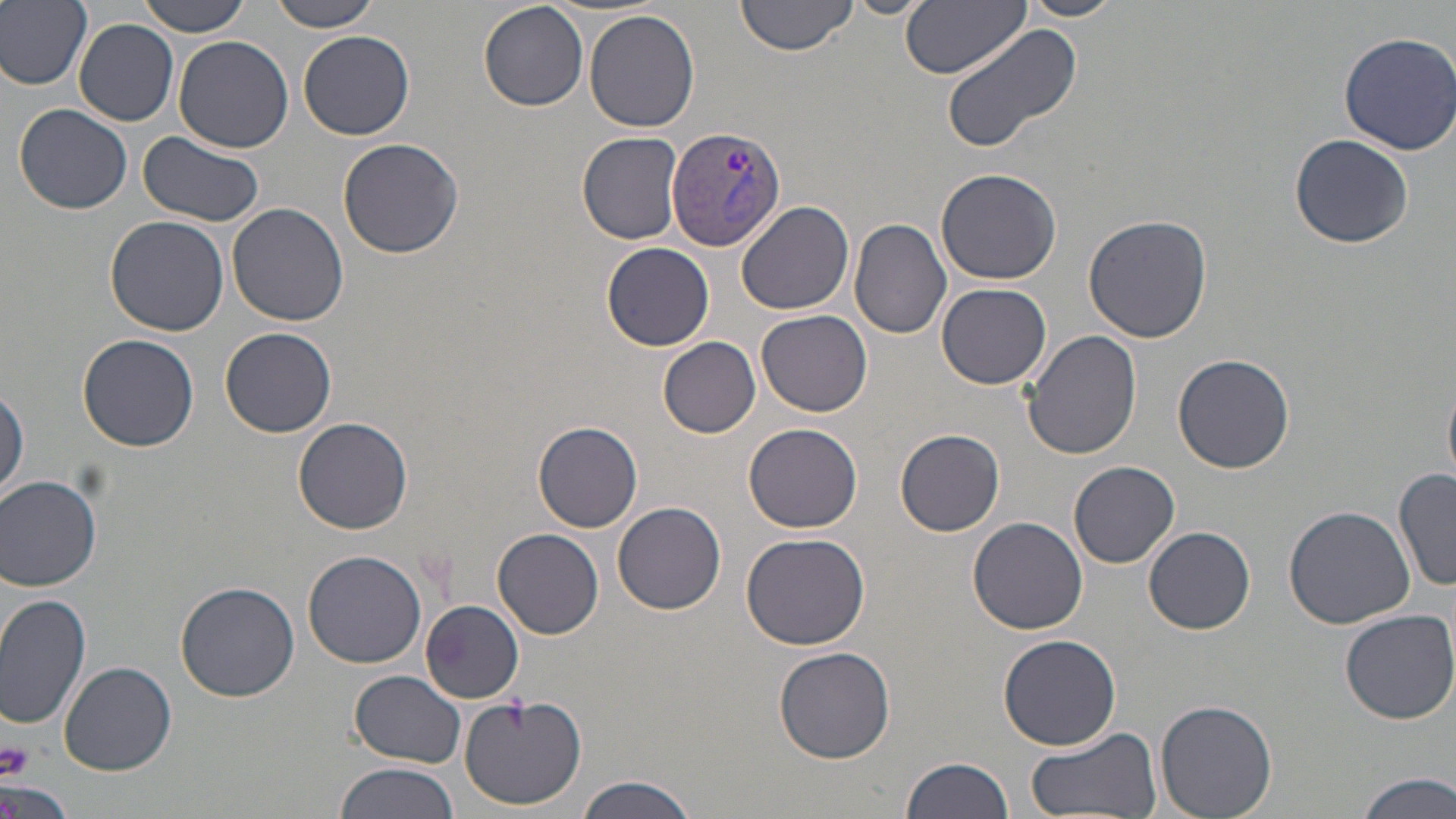

Approximate bounding boxes as (x1,y1)-(x2,y2) corner pairs in pixels. Uninfected red blood cell locations: (0,0)-(93,90), (135,0)-(254,36), (266,0)-(383,32), (736,0)-(858,56), (843,0)-(934,18), (902,0)-(1030,77), (1017,0)-(1128,21), (479,2)-(589,111), (585,8)-(701,133), (75,19)-(179,125), (941,22)-(1087,157), (299,29)-(415,140), (1337,32)-(1454,155), (172,35)-(293,153), (14,104)-(133,215), (139,131)-(267,227), (577,131)-(685,244), (1288,133)-(1414,248), (338,136)-(466,259), (935,169)-(1061,284), (736,201)-(855,315), (228,202)-(349,326), (1084,214)-(1212,343), (105,216)-(231,335), (849,216)-(953,340), (601,242)-(714,351), (937,282)-(1051,387), (755,308)-(873,418), (657,325)-(871,429), (221,327)-(336,437), (1025,332)-(1142,462), (78,334)-(200,452), (656,336)-(762,437), (1173,352)-(1295,474), (1443,379)-(1456,486), (1,380)-(28,502), (294,416)-(412,533), (531,421)-(644,533), (743,423)-(862,533), (894,429)-(1005,536), (1068,461)-(1180,569), (1395,467)-(1455,594), (0,473)-(103,591), (613,502)-(726,614), (1285,505)-(1415,630), (968,517)-(1089,636), (1144,526)-(1255,635), (493,529)-(604,640), (739,532)-(871,651), (302,549)-(427,668), (175,580)-(300,702), (0,593)-(93,733), (419,598)-(524,703), (1339,609)-(1456,725), (997,635)-(1123,751), (774,645)-(897,765), (59,659)-(178,775), (351,670)-(467,768), (456,693)-(588,810), (1155,699)-(1278,819), (1023,726)-(1163,818), (899,754)-(1017,819), (332,762)-(461,819), (1354,772)-(1456,819), (576,776)-(696,819), (0,779)-(74,819). Platelet locations: (1,739)-(33,780). Plasmodium vivax-infected red blood cell locations: (667,125)-(787,252). Slide-level diagnosis: Plasmodium vivax. One field of a larger specimen. 1000x magnification. May-Grünwald-Giemsa-stained preparation. Thin blood smear. Light microscopy. Image is 1456×819 pixels.